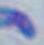 Toxoplasma gondii is shown. Photomicrograph. Captured at 1000x magnification.